Give a bounding box for every leukocyte visible.
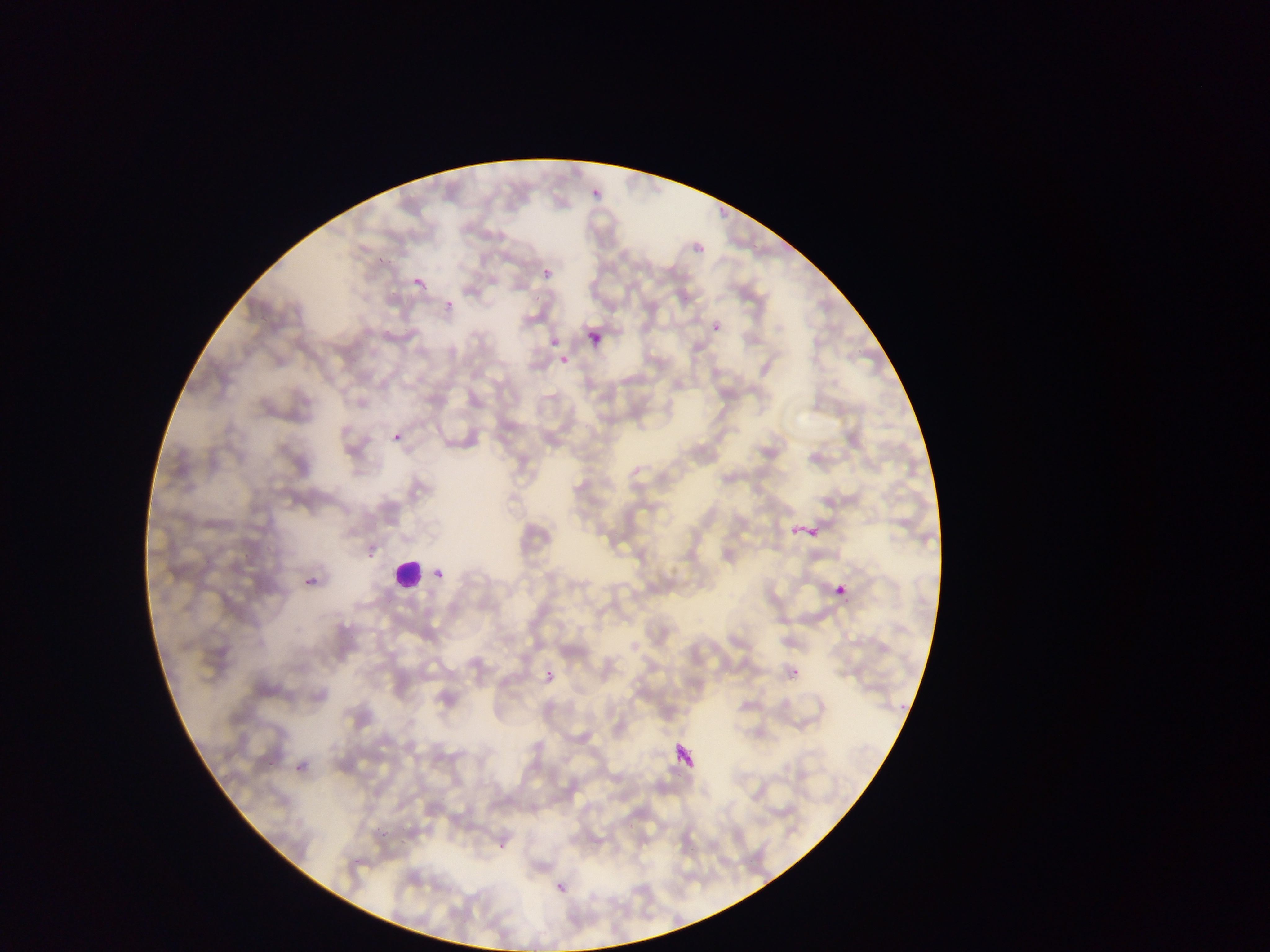

Approximate bounding boxes as [left, top, right, bottom] in pixels.
Leukocytes: [392, 555, 422, 589].

preparation: thin blood smear
field_of_view: single
image_size: 1270×952 pixels
country: Ghana
malaria_parasite_locations: 'approximate bounding boxes as [left, top, right, bottom] in pixels: [589, 187, 604, 202], [696, 244, 704, 253], [543, 268, 553, 278], [407, 273, 428, 284], [442, 303, 458, 319], [705, 326, 722, 336], [586, 329, 602, 346], [550, 338, 559, 348], [559, 355, 569, 364], [393, 433, 401, 441], [361, 553, 373, 560], [431, 567, 448, 586], [300, 572, 320, 588], [832, 582, 846, 597], [538, 660, 560, 681], [787, 661, 797, 676], [288, 765, 300, 782], [374, 831, 387, 841], [492, 837, 506, 854], [348, 856, 357, 869], [555, 880, 567, 899]'
capture: mobile-phone photograph through a microscope